Evaluate for Plasmodium parasites.
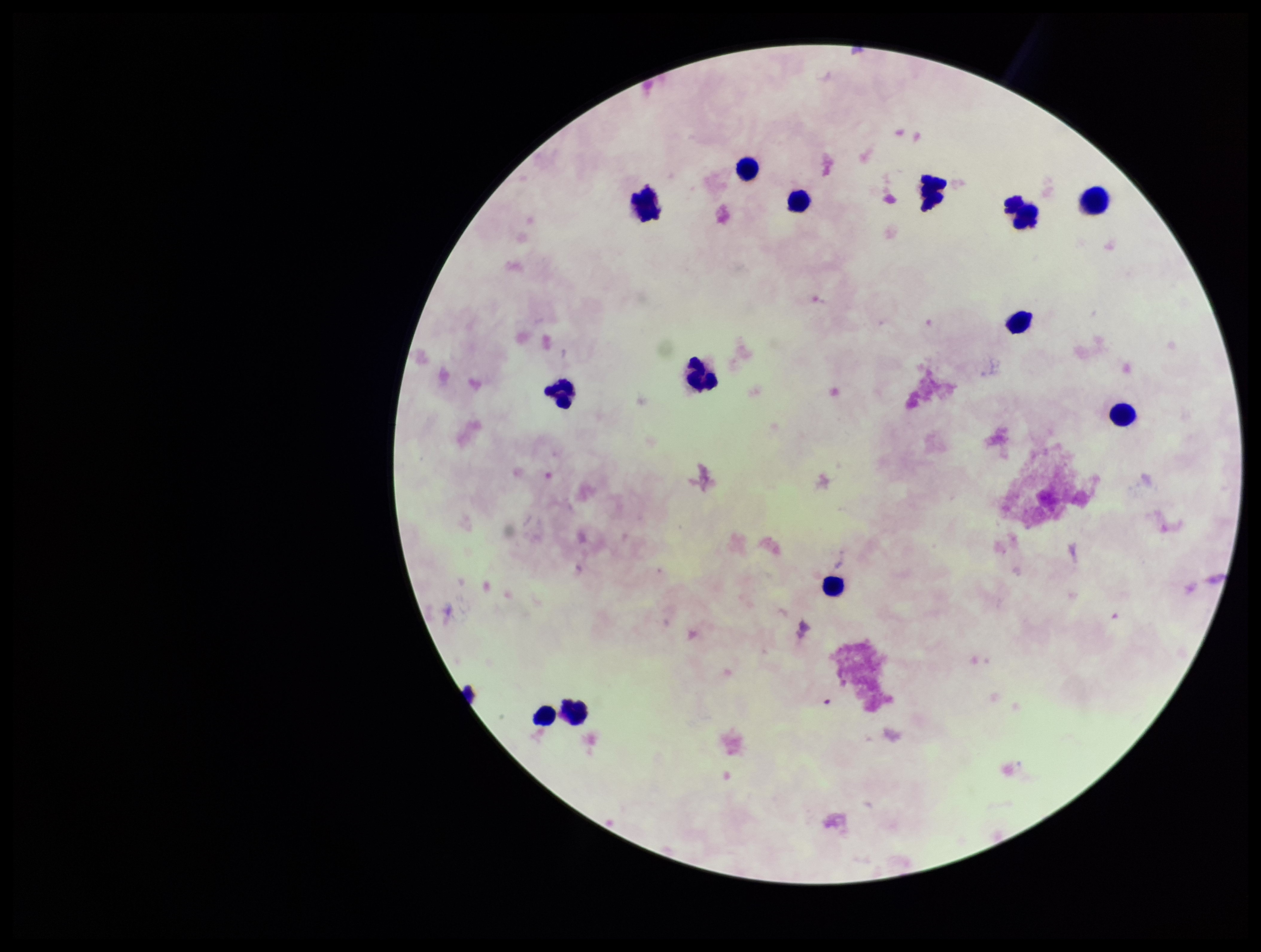

None seen.

Photographed through the microscope eyepiece with a smartphone camera. Parasite count: 0. Image is 1261×952 pixels. Stained with Giemsa. Preparation: thick smear. Single field of view. Patient malaria status: negative. Leukocyte count: 13.